Locate every uninfected red blood cell.
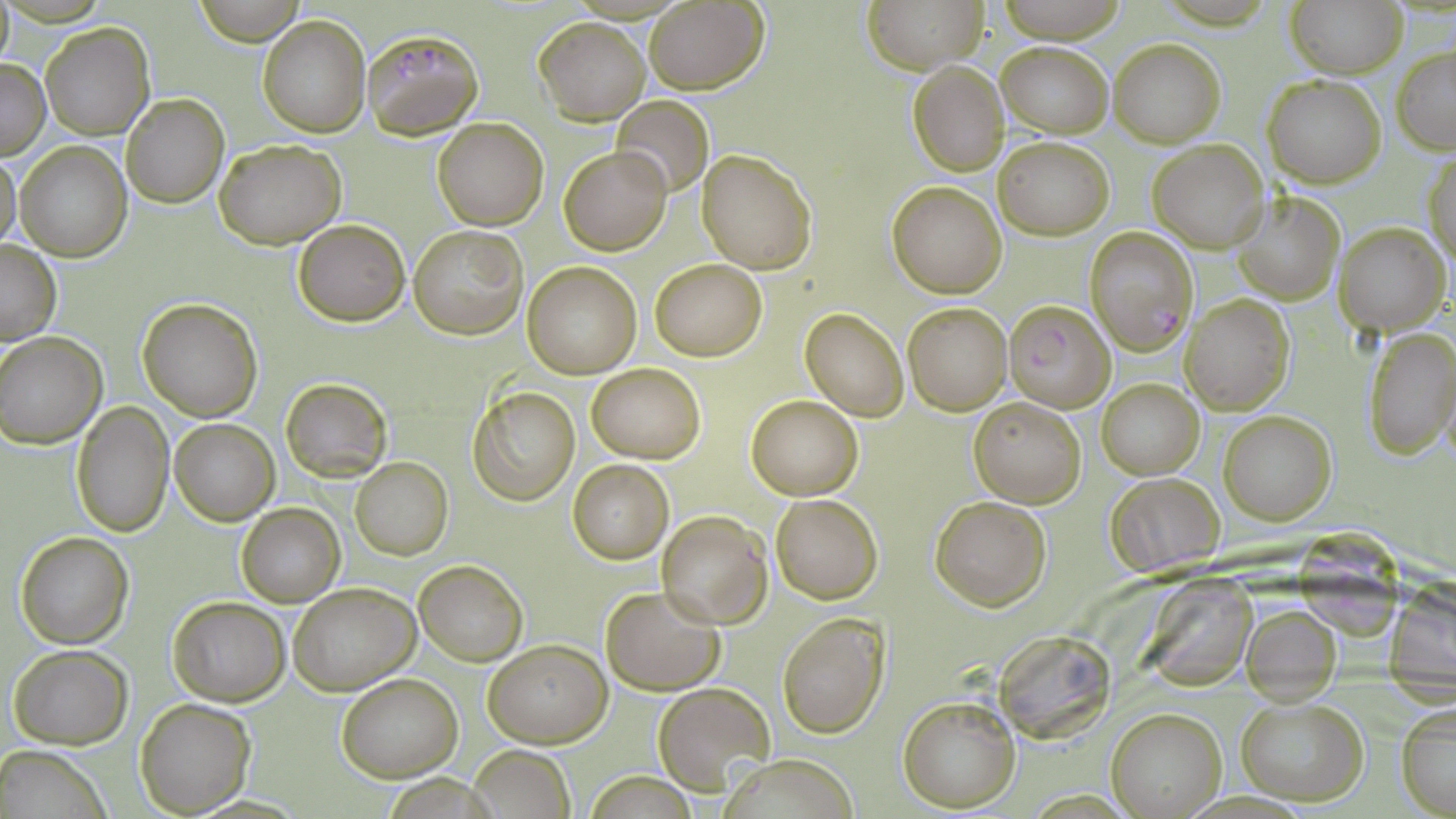
Approximate bounding boxes as named x1/y1/x2/y2 corners in pixels.
Uninfected red blood cells: (x1=863, y1=0, x2=989, y2=72), (x1=1286, y1=0, x2=1408, y2=77), (x1=190, y1=1, x2=309, y2=45), (x1=643, y1=2, x2=769, y2=93), (x1=258, y1=15, x2=370, y2=138), (x1=535, y1=17, x2=650, y2=124), (x1=41, y1=22, x2=155, y2=142), (x1=1110, y1=38, x2=1224, y2=148), (x1=996, y1=40, x2=1112, y2=138), (x1=1391, y1=45, x2=1456, y2=155), (x1=0, y1=59, x2=49, y2=158), (x1=908, y1=60, x2=1009, y2=176), (x1=1261, y1=74, x2=1385, y2=187), (x1=122, y1=94, x2=228, y2=208), (x1=611, y1=96, x2=714, y2=196), (x1=433, y1=118, x2=548, y2=230), (x1=992, y1=136, x2=1112, y2=239), (x1=1148, y1=138, x2=1269, y2=252), (x1=214, y1=139, x2=347, y2=249), (x1=15, y1=140, x2=132, y2=262), (x1=559, y1=145, x2=671, y2=256), (x1=698, y1=148, x2=817, y2=275), (x1=1425, y1=150, x2=1455, y2=273), (x1=0, y1=152, x2=23, y2=255), (x1=887, y1=181, x2=1007, y2=298), (x1=1236, y1=193, x2=1345, y2=305), (x1=292, y1=219, x2=409, y2=327), (x1=1334, y1=221, x2=1449, y2=336), (x1=408, y1=224, x2=527, y2=339), (x1=0, y1=241, x2=61, y2=345), (x1=650, y1=258, x2=767, y2=360), (x1=522, y1=262, x2=641, y2=378), (x1=1180, y1=296, x2=1295, y2=415), (x1=138, y1=298, x2=263, y2=422), (x1=901, y1=302, x2=1012, y2=414), (x1=800, y1=309, x2=909, y2=420), (x1=1363, y1=326, x2=1456, y2=460), (x1=0, y1=331, x2=107, y2=448), (x1=587, y1=363, x2=705, y2=463), (x1=280, y1=378, x2=392, y2=481), (x1=1097, y1=379, x2=1204, y2=480), (x1=468, y1=385, x2=580, y2=505), (x1=746, y1=395, x2=864, y2=501), (x1=969, y1=395, x2=1086, y2=508), (x1=70, y1=401, x2=173, y2=539), (x1=1220, y1=410, x2=1336, y2=525), (x1=170, y1=419, x2=278, y2=525), (x1=350, y1=457, x2=453, y2=559), (x1=568, y1=459, x2=674, y2=564), (x1=1104, y1=472, x2=1225, y2=577), (x1=770, y1=494, x2=883, y2=604), (x1=930, y1=494, x2=1050, y2=610), (x1=236, y1=503, x2=344, y2=606), (x1=656, y1=511, x2=772, y2=627), (x1=1299, y1=522, x2=1398, y2=644), (x1=15, y1=531, x2=134, y2=648), (x1=413, y1=560, x2=528, y2=666), (x1=1149, y1=570, x2=1258, y2=691), (x1=288, y1=581, x2=420, y2=695), (x1=1385, y1=582, x2=1455, y2=694), (x1=600, y1=586, x2=726, y2=695), (x1=167, y1=597, x2=289, y2=706), (x1=1240, y1=603, x2=1340, y2=702), (x1=777, y1=612, x2=891, y2=738), (x1=1003, y1=631, x2=1113, y2=747), (x1=483, y1=639, x2=610, y2=747), (x1=7, y1=645, x2=132, y2=748), (x1=336, y1=674, x2=462, y2=781), (x1=653, y1=683, x2=774, y2=794), (x1=1234, y1=693, x2=1370, y2=807), (x1=897, y1=694, x2=1020, y2=811), (x1=134, y1=697, x2=255, y2=816), (x1=1395, y1=700, x2=1455, y2=818), (x1=1106, y1=708, x2=1225, y2=817), (x1=3, y1=746, x2=115, y2=819), (x1=467, y1=746, x2=576, y2=819), (x1=718, y1=756, x2=865, y2=818), (x1=587, y1=772, x2=699, y2=817).

Plasmodium falciparum-infected red blood cell locations = approximate bounding boxes as named x1/y1/x2/y2 corners in pixels: (x1=363, y1=28, x2=484, y2=138), (x1=1085, y1=227, x2=1199, y2=353), (x1=1005, y1=300, x2=1116, y2=413)
slide-level diagnosis = Plasmodium falciparum
field of view = single
stain = May-Grünwald-Giemsa
magnification = 1000x
image size = 1456×819 pixels
preparation = thin blood film
modality = optical microscopy